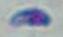 Photomicrograph. Toxoplasma gondii is shown. 1000x magnification.